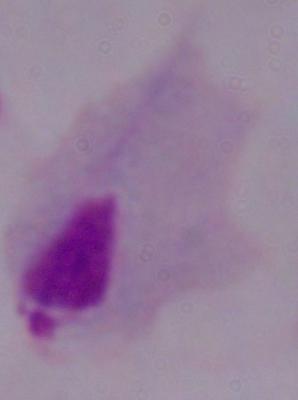
{
  "modality": "micrograph",
  "identification": "trichomonad",
  "magnification": "1000x"
}